Assess this cell for malaria.
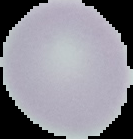
Uninfected.

image_size: 133×139 pixels
preparation: thin blood smear
image_type: segmented cell region on a black background